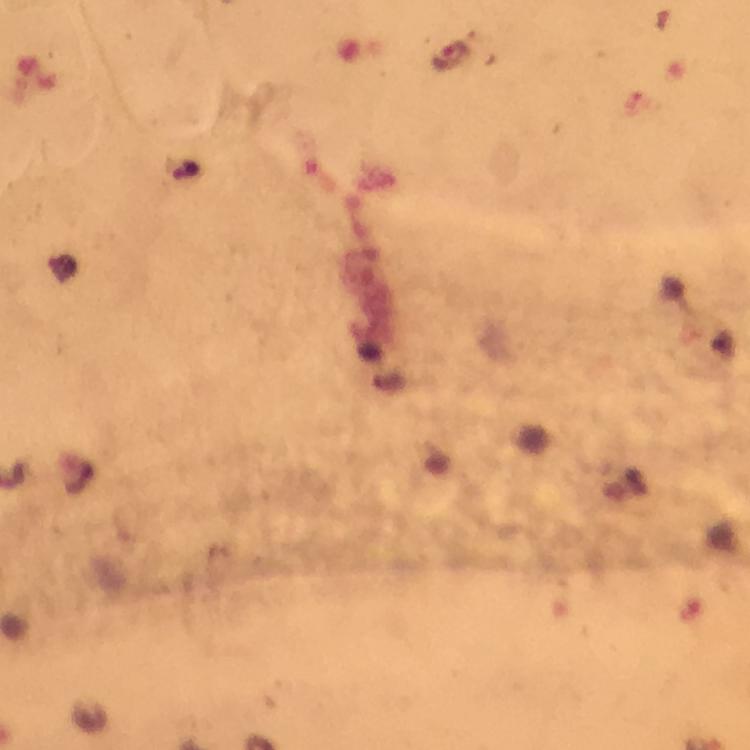

Approximate centers as {x, y} in pixels.
Summary:
  - Malaria parasite locations: {449, 57}
  - Image size: 750×750 pixels
  - Stain: Giemsa
  - Capture: smartphone camera through the microscope
  - Preparation: thick blood film
  - Immersion oil: applied
  - Cropped from: one field of view
  - Magnification: 100x
  - Context: from a diagnostic examination for malaria